Report the malaria status of this cell.
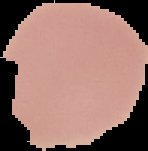
It is uninfected.

preparation = thin blood film
image size = 148×151 pixels
image type = cell region segmented out of the field of view; surrounding area masked to black